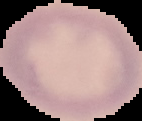

preparation = thin blood film
image size = 142×121 pixels
image type = cell region segmented out of the field of view; surrounding area masked to black
malaria status = uninfected